Assess this cell for malaria.
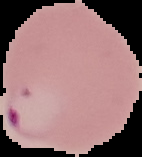
Parasitized.

Summary:
  - Preparation: thin blood film
  - Image size: 142×157 pixels
  - Image type: segmented cell region with the area outside set to black